Report the malaria status of this cell.
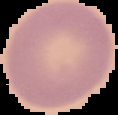
Uninfected.

image size = 118×115 pixels
preparation = thin blood smear
image type = cell region segmented out of the field of view; surrounding area masked to black